Identify the parasite.
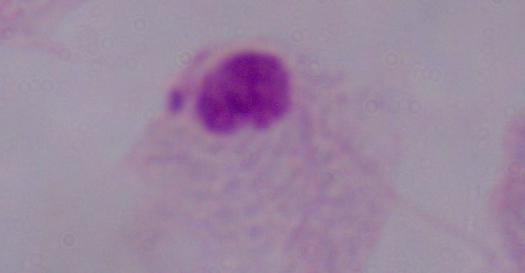
This is a trichomonad.

Micrograph. Captured at 1000x magnification.